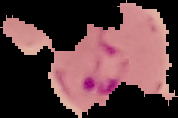
Malaria status: parasitized. From a thin blood smear. Image is 178×118 pixels. Cell region segmented out of the field of view; the surrounding area is masked to black.